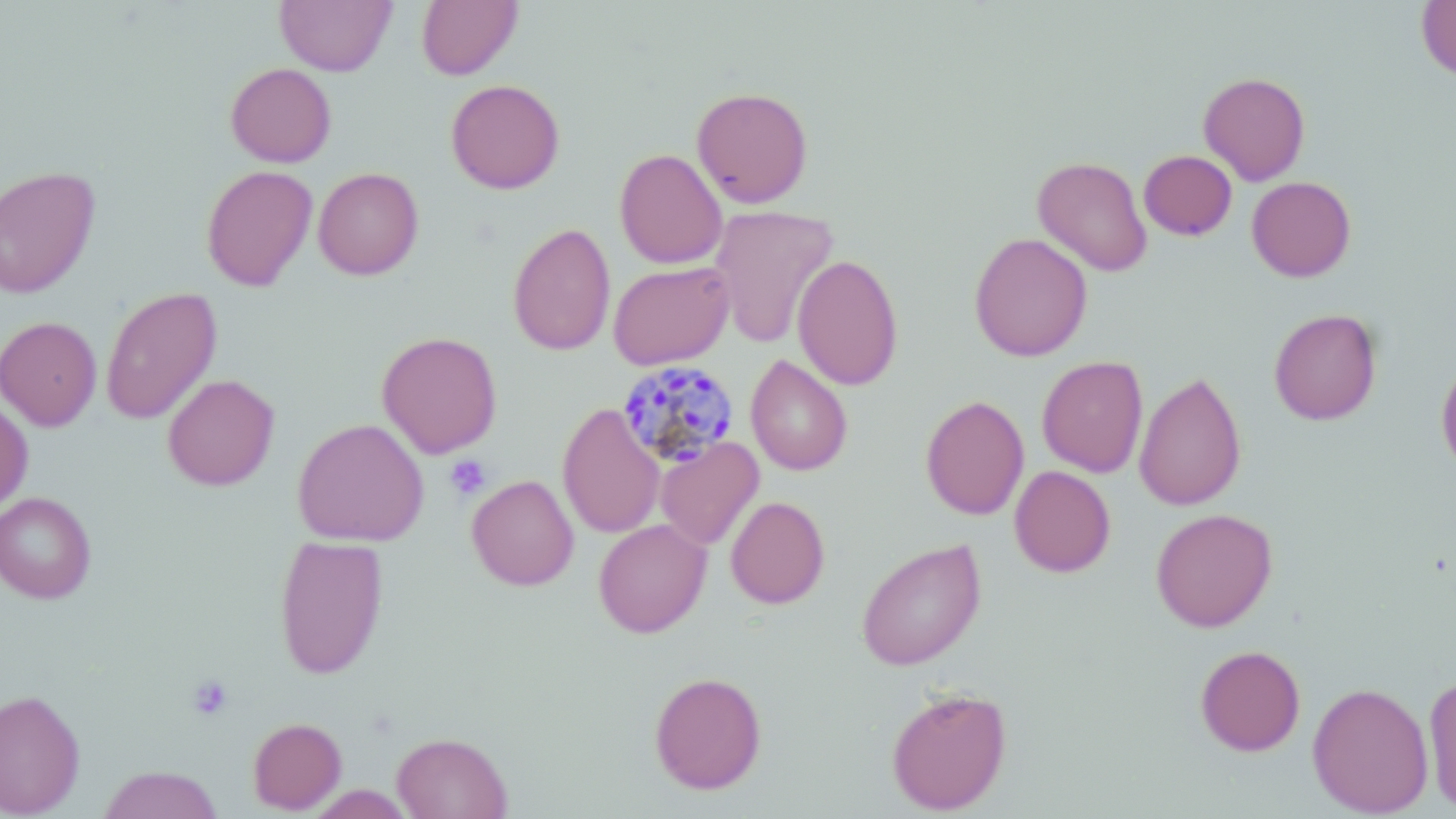
Summary:
  - Coordinate format: approximate bounding boxes as named x1/y1/x2/y2 corners in pixels
  - Uninfected red blood cell locations: (x1=274, y1=0, x2=396, y2=76), (x1=1416, y1=0, x2=1456, y2=81), (x1=416, y1=1, x2=523, y2=80), (x1=225, y1=62, x2=336, y2=167), (x1=1198, y1=71, x2=1311, y2=186), (x1=445, y1=79, x2=565, y2=194), (x1=692, y1=86, x2=814, y2=208), (x1=614, y1=148, x2=728, y2=269), (x1=1139, y1=150, x2=1237, y2=241), (x1=1031, y1=155, x2=1153, y2=276), (x1=201, y1=164, x2=318, y2=291), (x1=0, y1=165, x2=100, y2=299), (x1=312, y1=167, x2=424, y2=280), (x1=1246, y1=176, x2=1356, y2=281), (x1=708, y1=204, x2=839, y2=349), (x1=507, y1=222, x2=616, y2=356), (x1=969, y1=232, x2=1093, y2=361), (x1=792, y1=254, x2=904, y2=390), (x1=607, y1=260, x2=735, y2=369), (x1=101, y1=286, x2=222, y2=425), (x1=1268, y1=307, x2=1382, y2=425), (x1=0, y1=316, x2=102, y2=431), (x1=376, y1=331, x2=502, y2=458), (x1=745, y1=354, x2=853, y2=476), (x1=1036, y1=355, x2=1148, y2=478), (x1=1436, y1=355, x2=1456, y2=479), (x1=1133, y1=371, x2=1247, y2=511), (x1=162, y1=374, x2=279, y2=490), (x1=920, y1=395, x2=1029, y2=520), (x1=0, y1=396, x2=33, y2=512), (x1=557, y1=402, x2=665, y2=538), (x1=292, y1=418, x2=429, y2=546), (x1=656, y1=437, x2=764, y2=550), (x1=1009, y1=466, x2=1115, y2=577), (x1=466, y1=474, x2=579, y2=591), (x1=0, y1=492, x2=96, y2=603), (x1=725, y1=496, x2=830, y2=609), (x1=1150, y1=508, x2=1278, y2=632), (x1=593, y1=518, x2=711, y2=638), (x1=274, y1=534, x2=389, y2=679), (x1=856, y1=538, x2=987, y2=671), (x1=1195, y1=644, x2=1306, y2=756), (x1=648, y1=670, x2=767, y2=794), (x1=1423, y1=674, x2=1456, y2=813), (x1=1307, y1=681, x2=1434, y2=818), (x1=885, y1=685, x2=1012, y2=815), (x1=0, y1=688, x2=85, y2=818), (x1=247, y1=717, x2=346, y2=814), (x1=392, y1=732, x2=512, y2=819), (x1=98, y1=765, x2=223, y2=819), (x1=306, y1=785, x2=414, y2=818)
  - Plasmodium malariae-infected red blood cell locations: (x1=616, y1=360, x2=740, y2=468)
  - Platelet locations: (x1=445, y1=455, x2=491, y2=500), (x1=187, y1=675, x2=233, y2=721)
  - Slide-level diagnosis: Plasmodium malariae
  - Magnification: 1000x
  - Image size: 1456×819 pixels
  - Preparation: thin blood film
  - Modality: optical microscopy
  - Stain: May-Grünwald-Giemsa
  - Field of view: one of a larger specimen